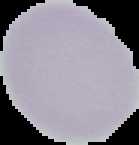

Summary:
  - Image type: segmented cell region with the area outside set to black
  - Preparation: thin blood film
  - Malaria status: uninfected
  - Image size: 139×145 pixels